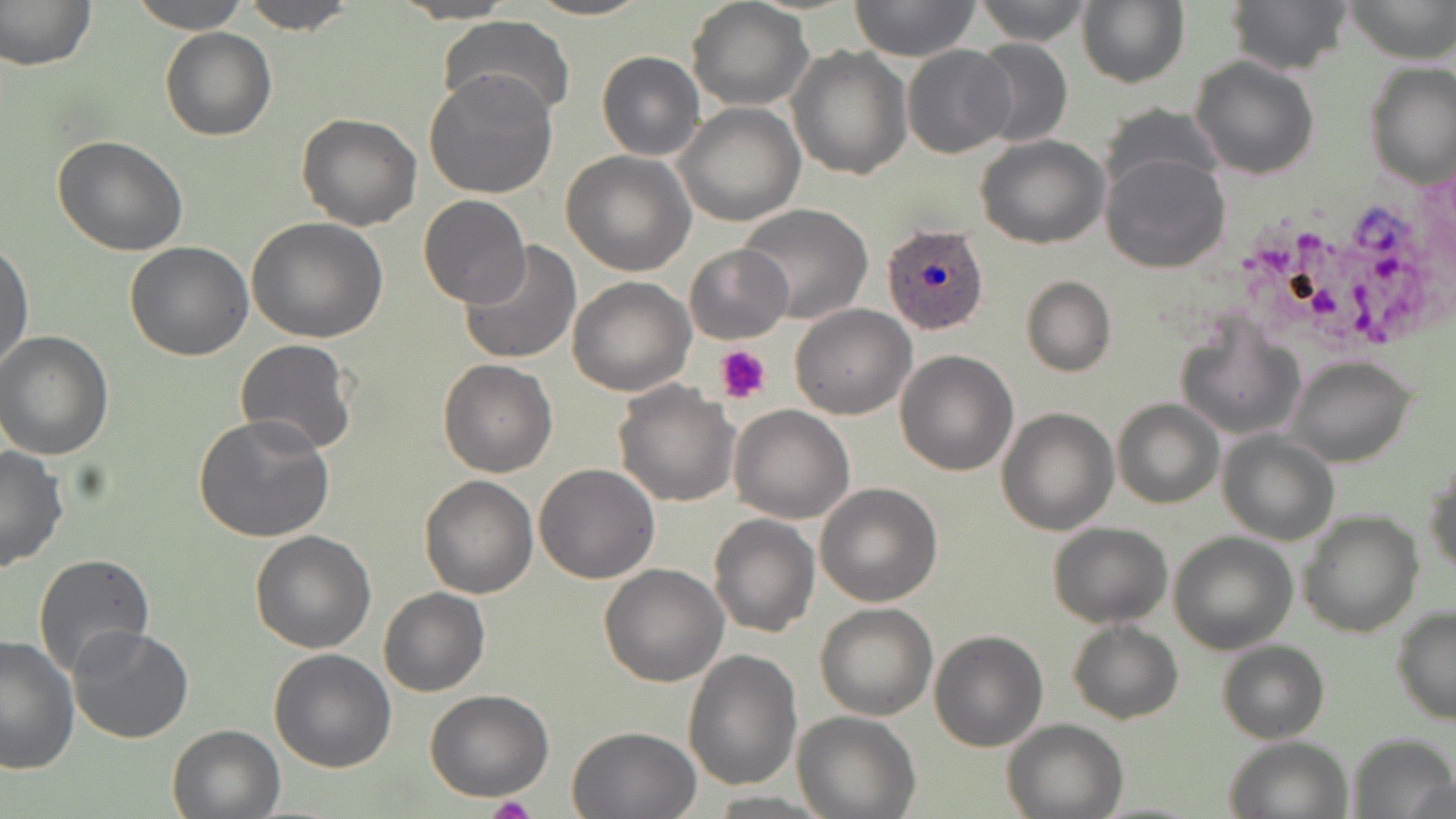
Summary:
  - Coordinate format: approximate bounding boxes as named x1/y1/x2/y2 corners in pixels
  - Uninfected red blood cell locations: (x1=128, y1=0, x2=252, y2=33), (x1=239, y1=0, x2=357, y2=35), (x1=388, y1=0, x2=518, y2=23), (x1=523, y1=0, x2=652, y2=21), (x1=849, y1=0, x2=982, y2=62), (x1=973, y1=0, x2=1094, y2=46), (x1=1079, y1=0, x2=1190, y2=89), (x1=1226, y1=0, x2=1354, y2=75), (x1=1344, y1=0, x2=1454, y2=63), (x1=1, y1=1, x2=98, y2=72), (x1=686, y1=1, x2=813, y2=109), (x1=437, y1=17, x2=576, y2=120), (x1=159, y1=27, x2=275, y2=142), (x1=967, y1=37, x2=1074, y2=150), (x1=902, y1=45, x2=1015, y2=157), (x1=787, y1=46, x2=911, y2=179), (x1=597, y1=51, x2=705, y2=161), (x1=1191, y1=56, x2=1319, y2=180), (x1=1365, y1=64, x2=1456, y2=188), (x1=425, y1=71, x2=558, y2=199), (x1=1099, y1=103, x2=1228, y2=198), (x1=674, y1=104, x2=804, y2=226), (x1=296, y1=111, x2=421, y2=230), (x1=51, y1=135, x2=190, y2=258), (x1=975, y1=135, x2=1109, y2=249), (x1=560, y1=151, x2=697, y2=277), (x1=1101, y1=153, x2=1231, y2=273), (x1=419, y1=195, x2=530, y2=308), (x1=737, y1=203, x2=873, y2=323), (x1=245, y1=217, x2=388, y2=342), (x1=457, y1=240, x2=584, y2=365), (x1=0, y1=241, x2=33, y2=374), (x1=124, y1=241, x2=253, y2=361), (x1=683, y1=243, x2=792, y2=344), (x1=1021, y1=275, x2=1115, y2=377), (x1=566, y1=276, x2=695, y2=396), (x1=789, y1=304, x2=915, y2=420), (x1=1175, y1=319, x2=1305, y2=441), (x1=0, y1=331, x2=116, y2=460), (x1=235, y1=339, x2=358, y2=456), (x1=895, y1=350, x2=1019, y2=476), (x1=1288, y1=355, x2=1417, y2=468), (x1=438, y1=359, x2=558, y2=477), (x1=612, y1=382, x2=740, y2=507), (x1=1113, y1=398, x2=1223, y2=509), (x1=729, y1=403, x2=855, y2=523), (x1=997, y1=407, x2=1119, y2=535), (x1=194, y1=412, x2=336, y2=542), (x1=1218, y1=430, x2=1339, y2=546), (x1=0, y1=446, x2=69, y2=573), (x1=1425, y1=451, x2=1456, y2=581), (x1=533, y1=463, x2=660, y2=584), (x1=420, y1=475, x2=538, y2=598), (x1=815, y1=482, x2=943, y2=607), (x1=1298, y1=510, x2=1423, y2=638), (x1=708, y1=513, x2=820, y2=638), (x1=1048, y1=522, x2=1172, y2=629), (x1=249, y1=530, x2=377, y2=653), (x1=1169, y1=531, x2=1298, y2=654), (x1=32, y1=554, x2=158, y2=680), (x1=599, y1=563, x2=729, y2=685), (x1=378, y1=587, x2=489, y2=696), (x1=815, y1=602, x2=937, y2=720), (x1=1392, y1=605, x2=1456, y2=724), (x1=1067, y1=619, x2=1183, y2=725), (x1=68, y1=625, x2=194, y2=745), (x1=929, y1=630, x2=1047, y2=751), (x1=0, y1=634, x2=80, y2=775), (x1=1217, y1=639, x2=1329, y2=744), (x1=268, y1=648, x2=397, y2=772), (x1=682, y1=648, x2=802, y2=791), (x1=425, y1=688, x2=552, y2=801), (x1=795, y1=711, x2=919, y2=819), (x1=1002, y1=718, x2=1130, y2=818), (x1=167, y1=722, x2=287, y2=818), (x1=566, y1=726, x2=701, y2=817), (x1=1348, y1=733, x2=1455, y2=819), (x1=1226, y1=737, x2=1351, y2=819)
  - Plasmodium ovale-infected red blood cell locations: (x1=882, y1=222, x2=990, y2=335)
  - Platelet locations: (x1=714, y1=344, x2=771, y2=405), (x1=485, y1=794, x2=537, y2=819)
  - Slide-level diagnosis: Plasmodium ovale
  - Stain: May-Grünwald-Giemsa
  - Image size: 1456×819 pixels
  - Preparation: thin blood film
  - Field of view: single
  - Magnification: 1000x
  - Modality: optical microscopy